Locate every Trypanosoma brucei.
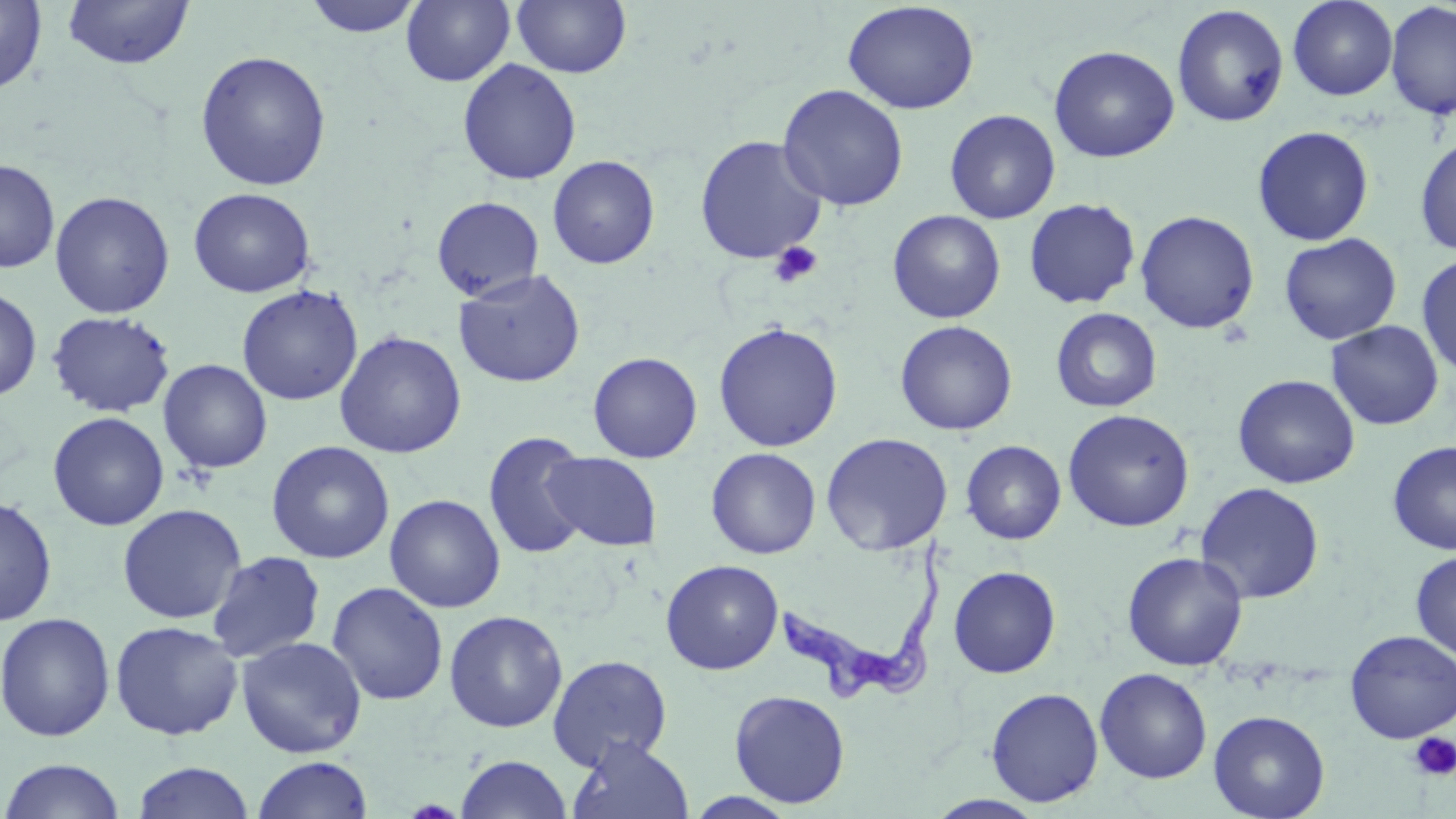
Approximate bounding boxes as (x1, y1, x2, y2) in pixels.
Trypanosoma brucei: (778, 537, 950, 702).

Summary:
  - Platelet locations: (769, 242, 823, 289), (1410, 732, 1456, 781)
  - Uninfected red blood cell locations: (301, 0, 425, 38), (401, 0, 515, 87), (511, 0, 631, 79), (1287, 0, 1398, 101), (0, 1, 47, 94), (62, 1, 194, 70), (842, 1, 980, 115), (1385, 2, 1456, 120), (1172, 4, 1289, 127), (1048, 45, 1179, 163), (195, 50, 332, 191), (457, 59, 582, 186), (777, 84, 909, 212), (944, 109, 1061, 224), (1252, 125, 1375, 246), (694, 135, 827, 265), (1414, 135, 1456, 256), (547, 155, 660, 270), (0, 158, 60, 273), (188, 188, 316, 298), (50, 190, 175, 319), (431, 196, 545, 302), (1024, 198, 1141, 309), (887, 210, 1006, 323), (1135, 210, 1260, 333), (1279, 233, 1402, 344), (1416, 254, 1456, 378), (453, 269, 585, 388), (237, 285, 363, 406), (0, 286, 42, 402), (1050, 307, 1161, 413), (46, 310, 176, 418), (895, 320, 1017, 436), (1326, 321, 1444, 431), (713, 322, 844, 452), (334, 330, 467, 459), (588, 351, 702, 463), (158, 359, 272, 474), (1232, 374, 1359, 489), (1062, 408, 1195, 532), (47, 411, 169, 531), (483, 432, 593, 560), (821, 432, 953, 555), (266, 440, 394, 564), (960, 440, 1066, 545), (1387, 440, 1456, 555), (705, 448, 821, 559), (544, 451, 662, 551), (1194, 482, 1325, 604), (384, 494, 505, 613), (0, 495, 58, 627), (117, 503, 247, 624), (206, 550, 327, 663), (1411, 551, 1456, 660), (1123, 552, 1248, 670), (661, 559, 783, 674), (948, 566, 1061, 678), (326, 581, 449, 706), (444, 610, 568, 733), (0, 612, 116, 742), (109, 620, 244, 741), (1344, 630, 1456, 743), (236, 636, 367, 759), (548, 655, 672, 770), (1094, 668, 1212, 783), (986, 687, 1104, 807), (729, 689, 850, 808), (1208, 710, 1330, 819), (567, 737, 693, 819), (456, 754, 572, 819), (251, 755, 374, 818), (2, 758, 126, 819), (132, 761, 254, 819), (682, 792, 801, 818), (925, 794, 1047, 818)
  - Slide-level diagnosis: Trypanosoma brucei
  - Field of view: single
  - Magnification: 1000x
  - Modality: light microscopy
  - Stain: May-Grünwald-Giemsa
  - Preparation: thin blood smear
  - Image size: 1456×819 pixels